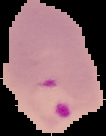
Summary:
  - Result: Plasmodium parasites identified
  - Preparation: thin blood smear
  - Image type: cell region segmented out of the field of view; surrounding area masked to black
  - Image size: 106×136 pixels